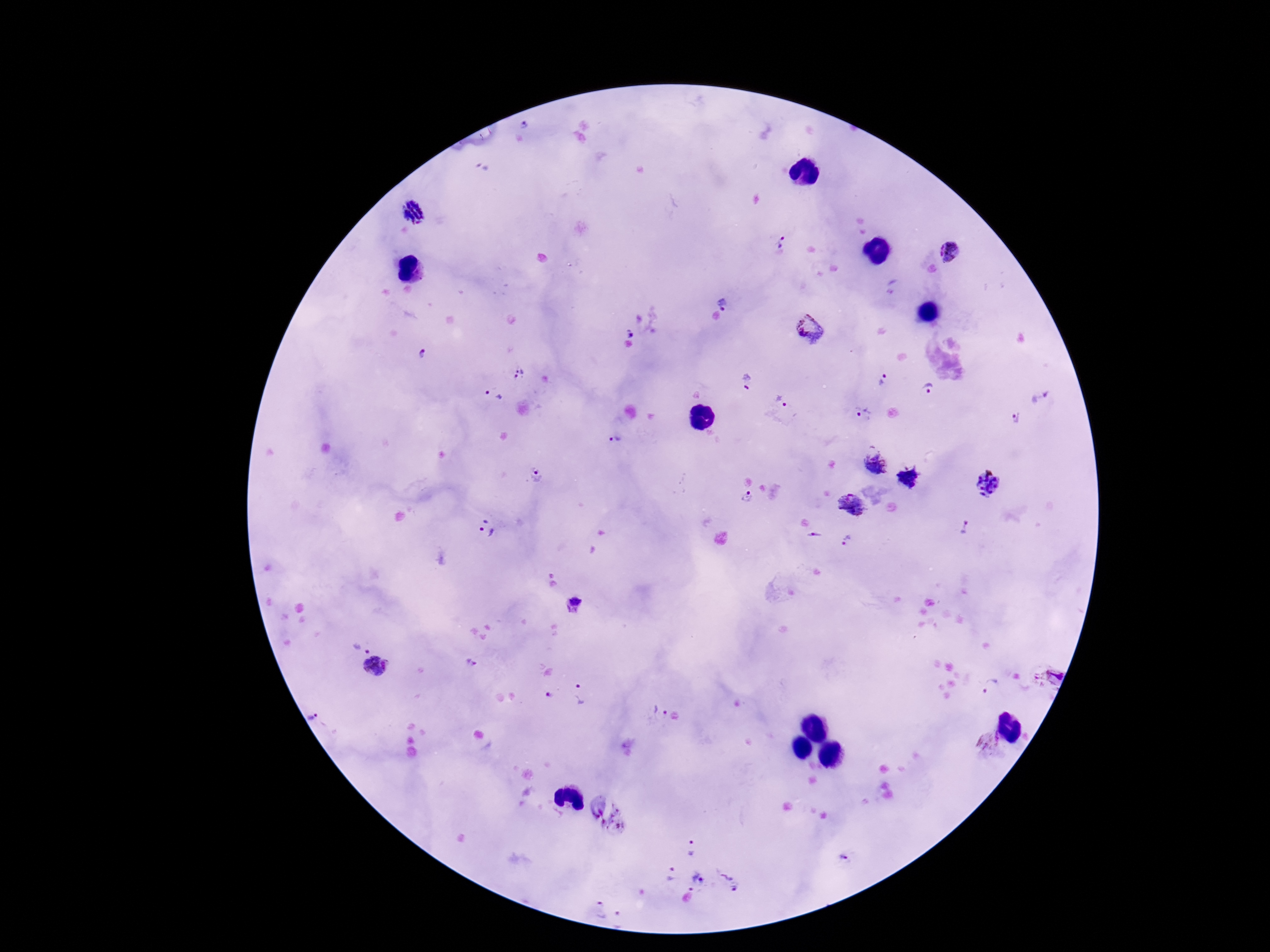
Approximate centers as (x, y) in pixels.
Summary:
  - Plasmodium parasite locations: (524, 125), (412, 211), (784, 242), (949, 253), (724, 300), (641, 322), (812, 328), (423, 353), (521, 374), (884, 380), (748, 381), (929, 387), (493, 396), (781, 401), (863, 413), (1017, 420), (614, 440), (873, 463), (536, 473), (910, 477), (988, 485), (749, 497), (850, 508), (965, 527), (487, 529), (813, 537), (847, 541), (574, 607), (360, 649), (470, 663), (377, 668), (1052, 675), (991, 685), (549, 690), (581, 693), (659, 713), (318, 715), (990, 745), (692, 846), (842, 858), (669, 873), (695, 883), (729, 884), (596, 910), (619, 920)
  - Field of view: one from this slide
  - Stain: Giemsa
  - Patient malaria status: positive
  - Magnification: 100x
  - Preparation: thick blood smear
  - Capture: smartphone camera through the microscope eyepiece
  - Image size: 1270×952 pixels